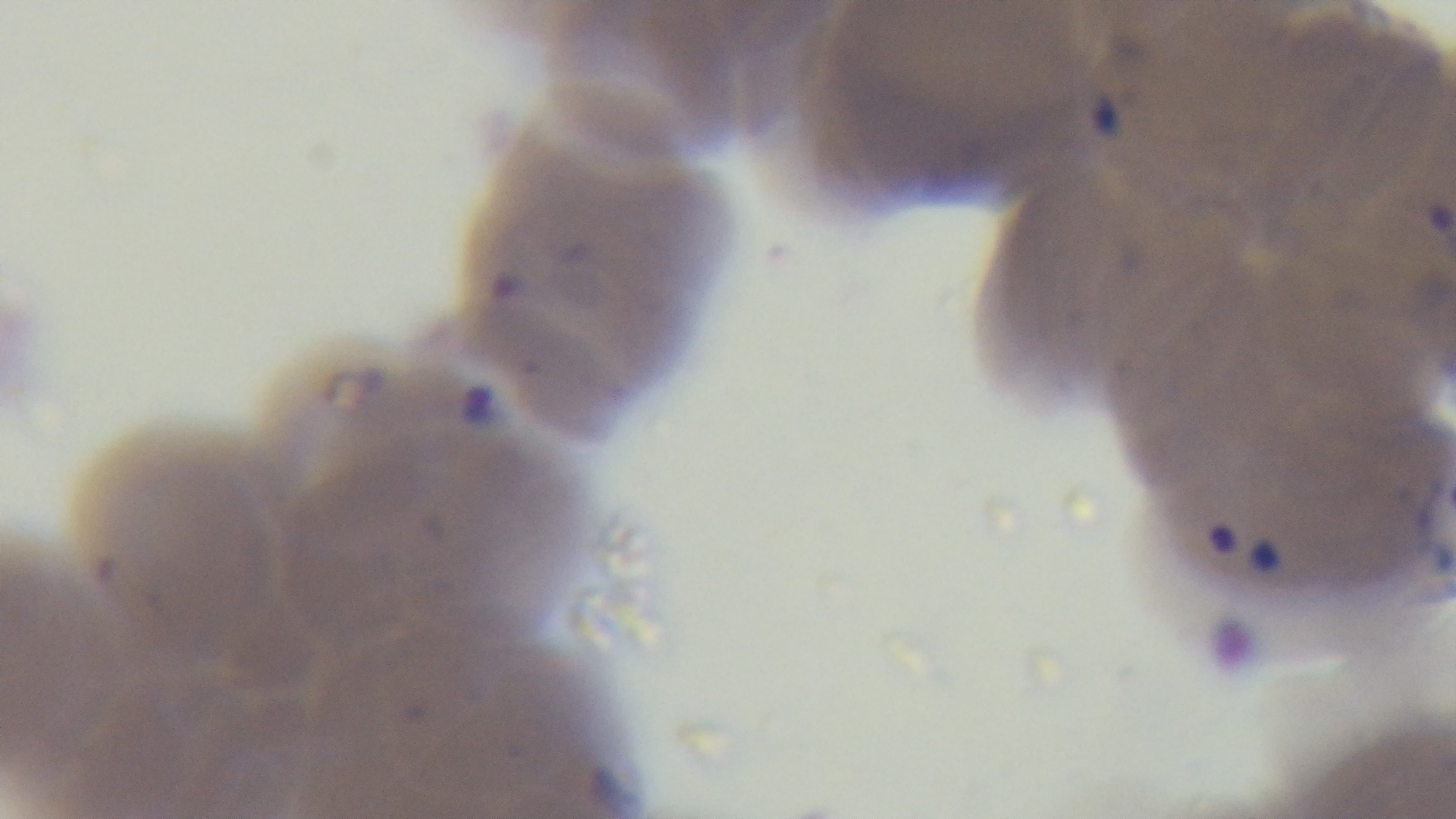
{
  "stain": "Giemsa",
  "objective": "100x oil immersion",
  "capture": "mounted 4K digital camera",
  "modality": "light microscopy",
  "malaria_status": "infected",
  "preparation": "thin",
  "field_of_view": "single"
}